Report the malaria status of this cell.
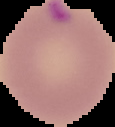
It is parasitized.

image type = cell region segmented out of the field of view; surrounding area masked to black
image size = 115×127 pixels
preparation = thin blood smear